State which cell type is depicted.
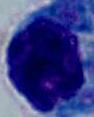

A leukocyte.

modality = micrograph
magnification = 1000x